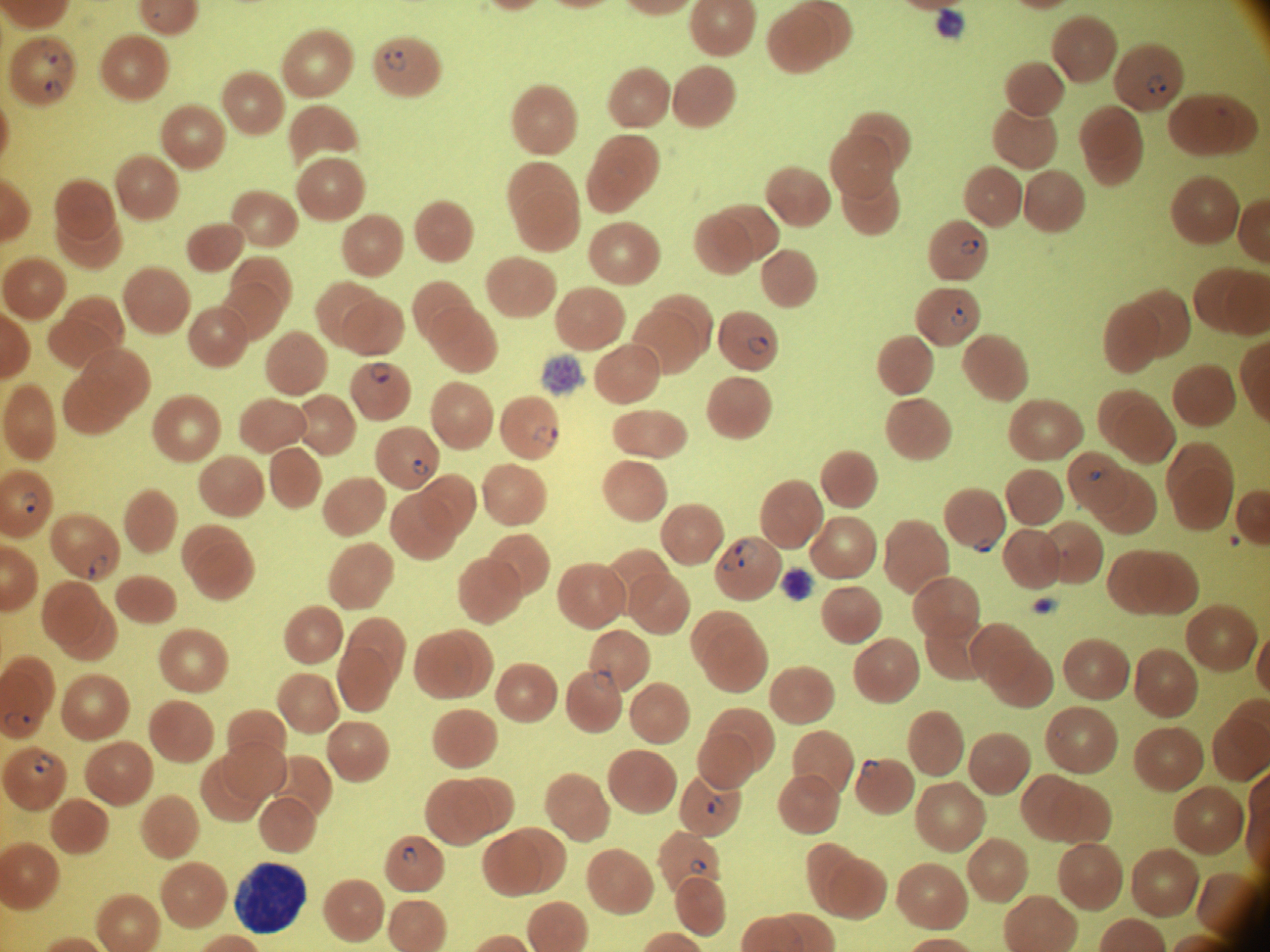
microscope = Leica DM2000 with built-in camera
field of view = one from this slide
species = Plasmodium falciparum
image size = 1270×952 pixels
stain = Giemsa
magnification = 100x
preparation = thin blood film
ring form locations = approximate bounding boxes as (x1, y1, x2, y2) in pixels, from the source annotation, which is not necessarily exhaustive: (385, 48, 406, 72), (49, 53, 71, 73), (1148, 74, 1166, 94), (45, 79, 66, 100), (960, 239, 980, 255), (951, 306, 969, 326), (747, 337, 770, 355), (370, 361, 391, 383), (533, 425, 558, 447), (411, 458, 429, 476), (1089, 471, 1100, 482), (21, 492, 39, 513), (973, 539, 995, 554), (735, 540, 759, 568), (89, 554, 109, 579), (592, 670, 614, 691), (3, 713, 30, 729), (33, 754, 53, 774), (860, 759, 880, 777), (707, 797, 726, 816), (402, 846, 417, 864), (690, 859, 707, 874)